Outline each uninfected red blood cell.
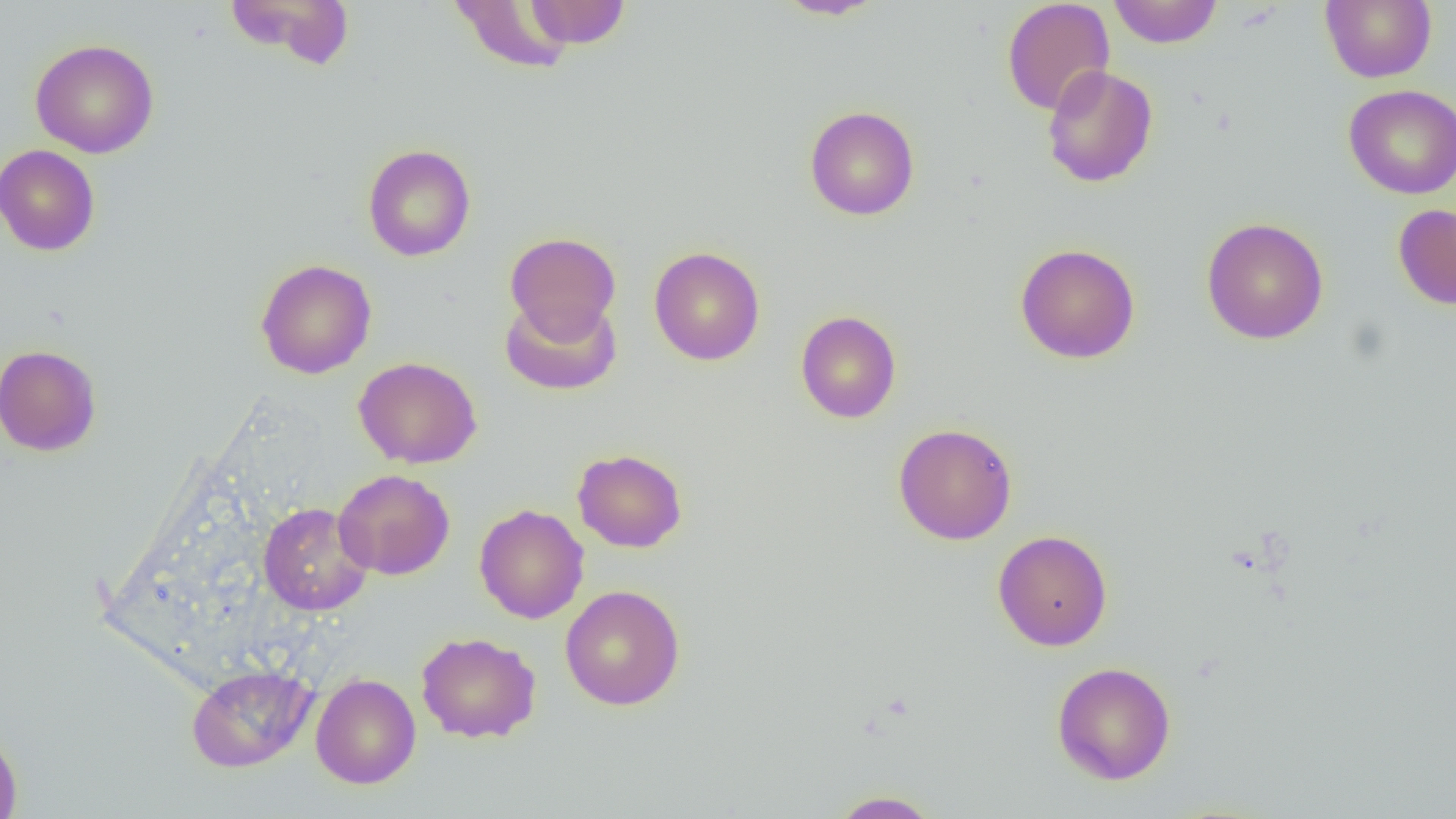

Approximate bounding boxes as named x1/y1/x2/y2 corners in pixels.
Uninfected red blood cells: (x1=225, y1=0, x2=356, y2=70), (x1=448, y1=0, x2=578, y2=75), (x1=522, y1=0, x2=632, y2=49), (x1=773, y1=0, x2=886, y2=20), (x1=1001, y1=0, x2=1115, y2=116), (x1=1107, y1=0, x2=1224, y2=48), (x1=1321, y1=0, x2=1437, y2=83), (x1=30, y1=39, x2=159, y2=158), (x1=1042, y1=65, x2=1158, y2=188), (x1=1343, y1=84, x2=1456, y2=199), (x1=805, y1=105, x2=920, y2=221), (x1=0, y1=144, x2=101, y2=256), (x1=362, y1=144, x2=476, y2=261), (x1=1393, y1=204, x2=1456, y2=310), (x1=1201, y1=217, x2=1329, y2=345), (x1=505, y1=232, x2=621, y2=340), (x1=1014, y1=243, x2=1140, y2=363), (x1=648, y1=246, x2=765, y2=365), (x1=255, y1=259, x2=377, y2=379), (x1=499, y1=294, x2=622, y2=396), (x1=795, y1=310, x2=902, y2=424), (x1=0, y1=344, x2=102, y2=457), (x1=353, y1=356, x2=482, y2=469), (x1=893, y1=423, x2=1017, y2=544), (x1=572, y1=448, x2=688, y2=553), (x1=333, y1=469, x2=455, y2=580), (x1=258, y1=502, x2=373, y2=616), (x1=474, y1=504, x2=589, y2=624), (x1=993, y1=529, x2=1112, y2=651), (x1=560, y1=585, x2=685, y2=710), (x1=415, y1=631, x2=542, y2=743), (x1=1051, y1=661, x2=1176, y2=785), (x1=186, y1=664, x2=317, y2=772), (x1=311, y1=673, x2=421, y2=788), (x1=0, y1=727, x2=23, y2=819), (x1=828, y1=790, x2=943, y2=818).

{
  "slide_level_diagnosis": "negative for blood parasites",
  "field_of_view": "one of a larger specimen",
  "magnification": "1000x",
  "image_size": "1456×819 pixels",
  "modality": "light microscopy",
  "preparation": "thin blood smear"
}